Give the position of every malaria parasite.
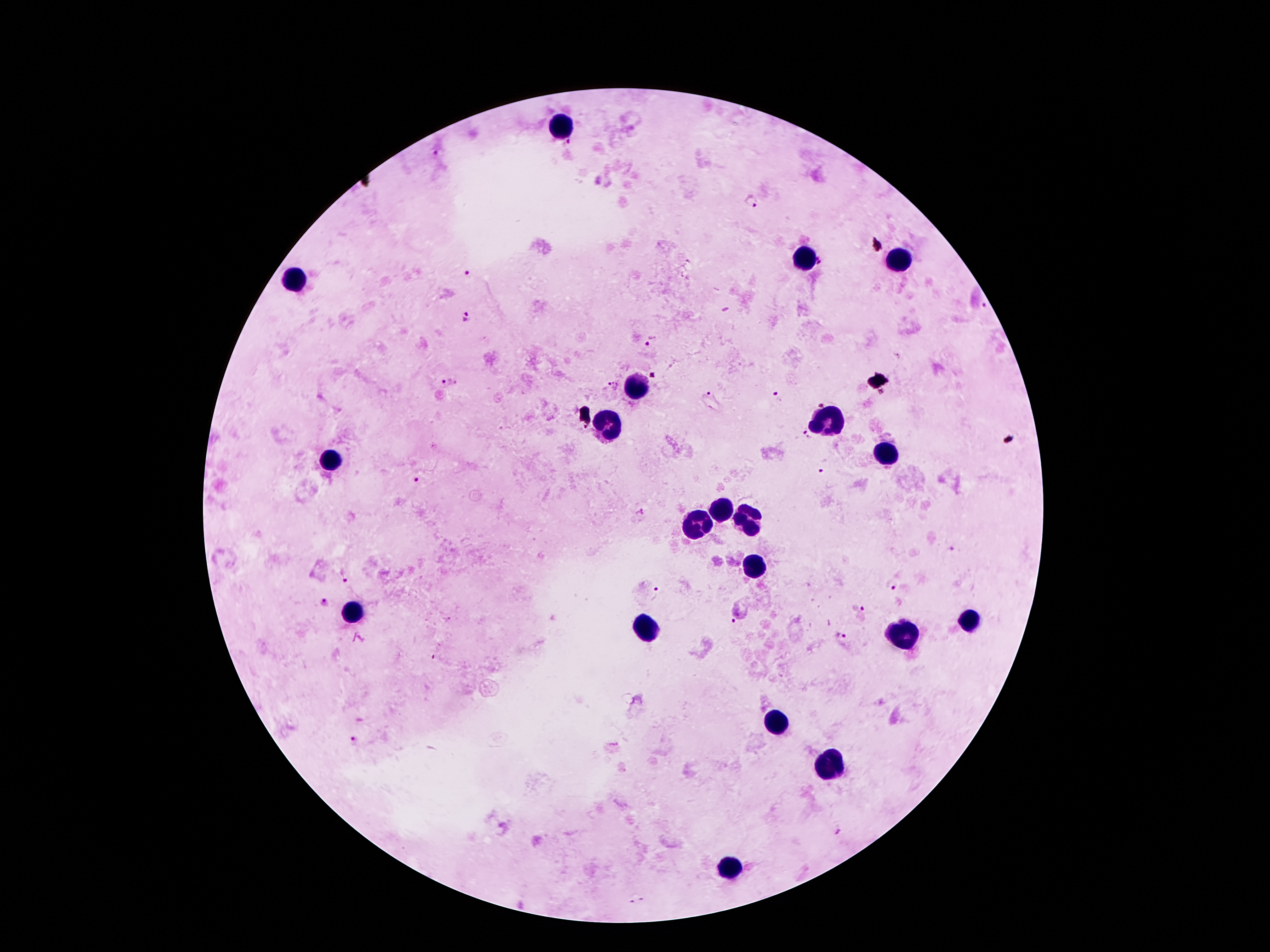

Approximate centers as {x, y} in pixels.
Malaria parasites: {569, 144}, {437, 153}, {751, 202}, {468, 275}, {984, 305}, {466, 318}, {652, 341}, {653, 376}, {442, 382}, {456, 383}, {611, 387}, {711, 393}, {775, 393}, {820, 404}, {805, 435}, {823, 472}, {417, 478}, {950, 549}, {342, 577}, {891, 585}, {659, 589}, {326, 602}, {857, 608}, {734, 620}, {841, 636}, {354, 741}, {838, 831}, {643, 900}, {631, 902}.

Leukocyte locations: {563, 126}, {895, 255}, {799, 260}, {297, 278}, {634, 389}, {831, 421}, {611, 427}, {888, 457}, {329, 459}, {718, 514}, {749, 516}, {695, 525}, {752, 568}, {354, 611}, {965, 623}, {647, 627}, {899, 636}, {779, 723}, {829, 766}, {727, 868}. Thick peripheral-blood smear. Smartphone photograph taken through the microscope eyepiece. One field from this slide. Giemsa-stained preparation. 100x magnification. Image is 1270×952 pixels. Patient malaria status: infected with Plasmodium falciparum.